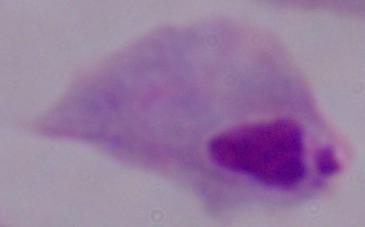
modality = micrograph
magnification = 1000x
identification = trichomonad